Classify this cell by malaria status.
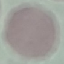

Uninfected.

Giemsa stain. Automatically extracted cell patch, resized to 64 × 64 pixels. Thin smear of blood. Acquired by smartphone through the microscope eyepiece.